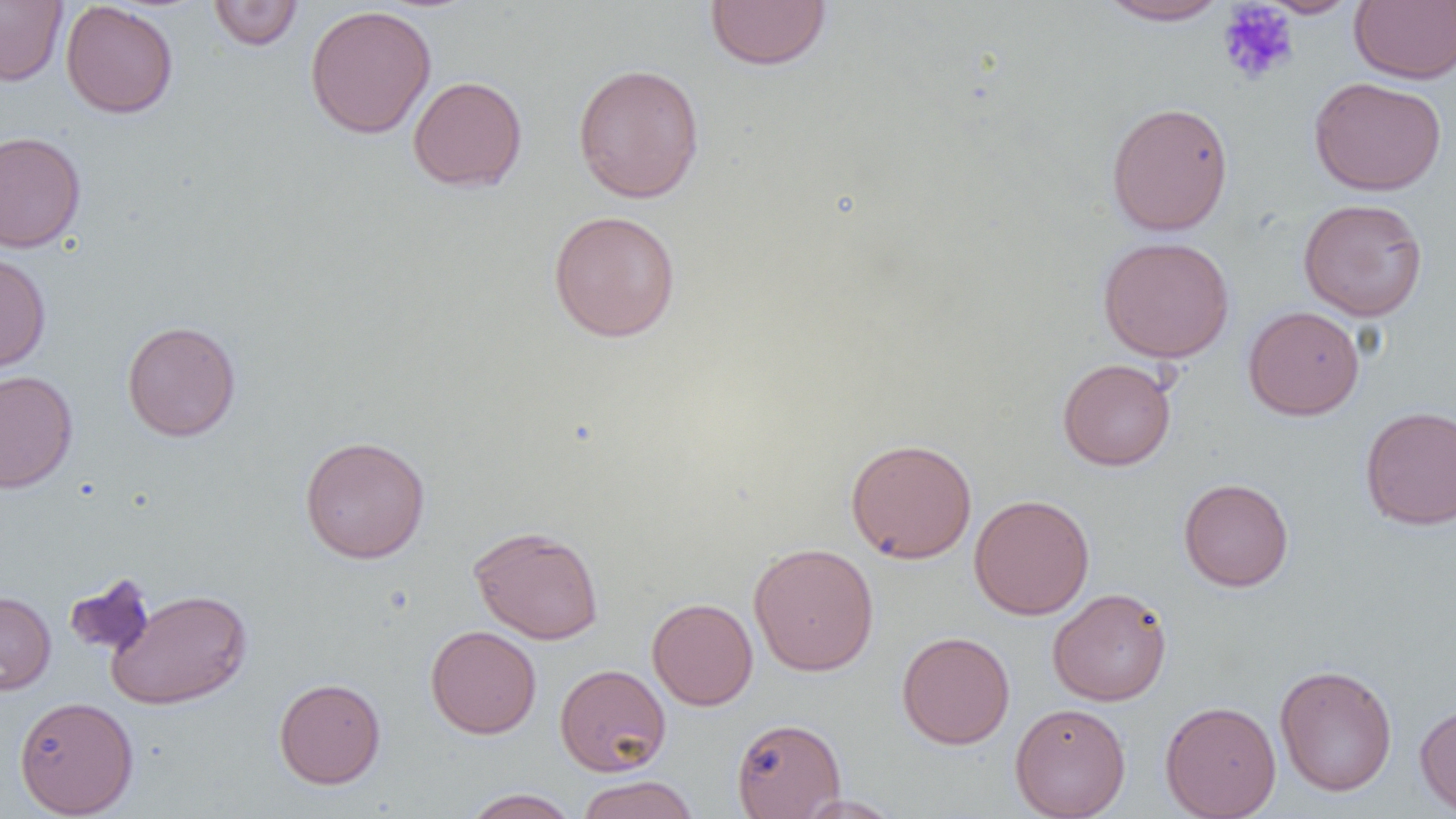

slide-level diagnosis = no evidence of blood parasites
field of view = one of a larger specimen
magnification = 1000x
preparation = thin blood film
modality = optical microscopy
image size = 1456×819 pixels
platelet locations = approximate bounding boxes as (x1,y1)-(x2,y2) corner pairs in pixels: (1216,2)-(1300,87)
uninfected red blood cell locations = approximate bounding boxes as (x1,y1)-(x2,y2) corner pairs in pixels: (704,0)-(832,71), (1097,0)-(1231,26), (1257,0)-(1360,18), (0,1)-(68,86), (207,1)-(304,51), (1349,1)-(1456,85), (60,2)-(179,118), (304,5)-(437,139), (572,62)-(706,204), (408,76)-(528,192), (1308,76)-(1447,196), (1105,101)-(1234,237), (0,131)-(86,253), (1298,197)-(1428,321), (548,209)-(681,343), (1097,235)-(1235,363), (0,252)-(51,373), (1243,305)-(1365,420), (121,319)-(241,441), (1058,358)-(1176,471), (0,369)-(78,493), (1359,405)-(1456,530), (300,435)-(431,564), (845,438)-(977,564), (1178,477)-(1294,591), (968,494)-(1095,620), (469,524)-(604,644), (748,542)-(879,676), (64,572)-(156,659), (1047,587)-(1173,706), (106,588)-(253,709), (0,590)-(56,695), (646,597)-(758,710), (425,625)-(541,738), (896,631)-(1015,749), (555,663)-(671,776), (1274,664)-(1398,797), (274,677)-(386,789), (13,695)-(139,817), (1414,698)-(1456,816), (1159,700)-(1281,819), (1010,702)-(1131,819), (731,717)-(846,818), (576,775)-(699,819), (461,788)-(581,819), (793,795)-(903,818)